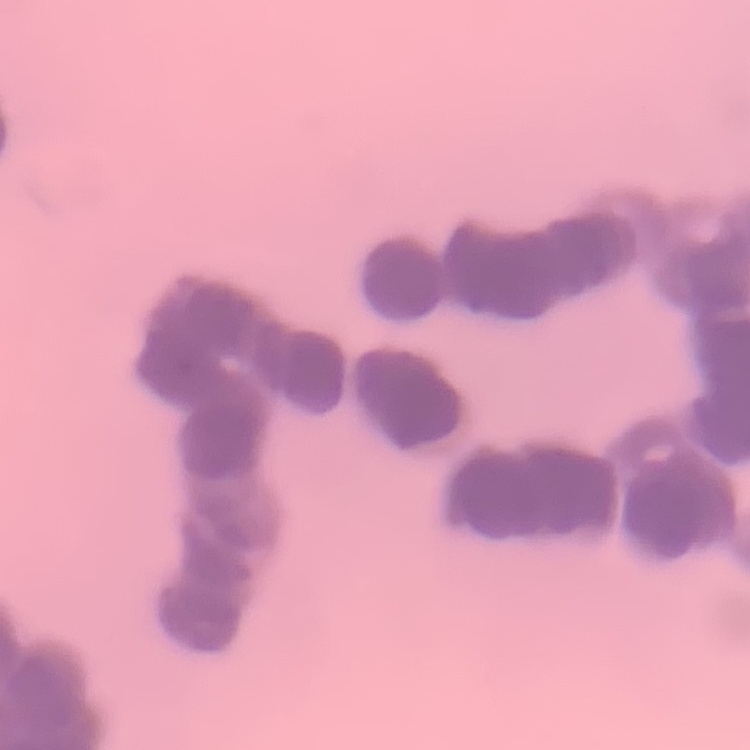
red_blood_cell_morphology: rouleaux formation
stain: Field's or Giemsa
preparation: thin blood smear
image_type: one tile cut from a larger photomicrograph